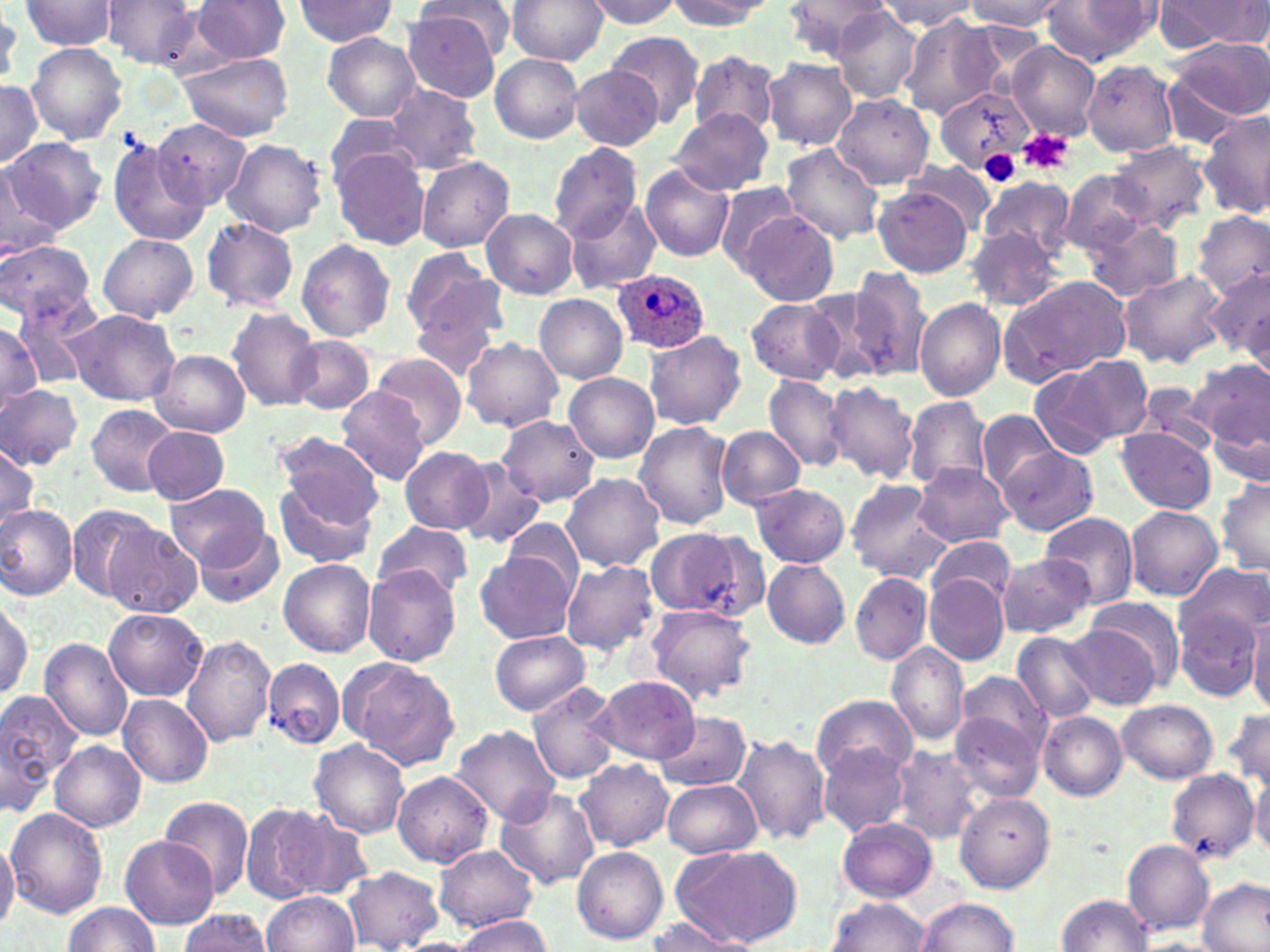

slide_level_diagnosis: Plasmodium ovale
uninfected_red_blood_cell_locations: 'approximate bounding boxes as [x1, y1, x2, y2] in pixels: [19, 0, 120, 53], [102, 0, 199, 67], [192, 0, 289, 62], [294, 0, 396, 45], [418, 0, 519, 52], [506, 0, 608, 64], [583, 0, 679, 27], [663, 0, 769, 31], [782, 0, 891, 59], [881, 0, 976, 30], [963, 0, 1065, 30], [1156, 0, 1268, 51], [1039, 1, 1157, 66], [834, 7, 920, 102], [403, 13, 504, 102], [899, 15, 1004, 118], [323, 31, 422, 122], [607, 32, 703, 126], [1168, 37, 1270, 125], [1005, 41, 1102, 139], [26, 43, 128, 145], [690, 50, 778, 139], [177, 52, 294, 140], [490, 54, 583, 143], [764, 58, 857, 150], [1083, 61, 1179, 157], [568, 65, 663, 151], [0, 80, 45, 171], [387, 84, 481, 174], [937, 87, 1035, 171], [833, 94, 934, 188], [670, 109, 773, 195], [1200, 111, 1270, 221], [324, 115, 414, 190], [152, 119, 252, 211], [106, 133, 208, 251], [3, 136, 103, 234], [223, 139, 326, 237], [548, 143, 644, 239], [778, 143, 885, 246], [1107, 143, 1208, 232], [331, 148, 431, 248], [416, 156, 515, 253], [902, 160, 1000, 233], [640, 165, 735, 261], [0, 168, 61, 258], [1058, 170, 1148, 255], [978, 175, 1073, 258], [712, 183, 804, 270], [873, 186, 973, 278], [564, 195, 661, 295], [481, 209, 578, 299], [1194, 209, 1270, 302], [742, 211, 839, 305], [202, 218, 300, 312], [1081, 220, 1184, 301], [965, 227, 1064, 310], [98, 233, 199, 322], [295, 239, 395, 342], [1, 240, 95, 322], [403, 247, 503, 341], [848, 266, 931, 379], [1206, 267, 1268, 363], [1118, 268, 1228, 369], [1000, 277, 1132, 385], [798, 287, 897, 384], [11, 290, 100, 386], [536, 294, 627, 385], [746, 299, 843, 384], [915, 299, 1006, 401], [408, 302, 502, 382], [228, 307, 321, 410], [64, 309, 180, 406], [0, 320, 41, 417], [645, 331, 746, 430], [287, 335, 375, 414], [461, 338, 564, 433], [153, 350, 250, 436], [373, 353, 467, 450], [1065, 354, 1154, 442], [1191, 359, 1270, 452], [1030, 365, 1123, 460], [566, 374, 659, 463], [763, 375, 852, 472], [821, 382, 918, 483], [0, 383, 83, 469], [1133, 383, 1219, 454], [336, 387, 429, 484], [904, 396, 991, 492], [86, 404, 182, 495], [1207, 406, 1269, 488], [978, 409, 1064, 492], [498, 415, 600, 506], [634, 421, 733, 530], [718, 425, 804, 509], [144, 426, 229, 505], [1116, 429, 1215, 513], [273, 431, 386, 525], [0, 445, 40, 538], [400, 446, 493, 534], [998, 447, 1098, 535], [455, 461, 547, 550], [913, 464, 1012, 547], [562, 472, 663, 571], [274, 479, 378, 568], [844, 479, 951, 583], [1215, 479, 1270, 578], [751, 483, 849, 568], [168, 484, 270, 569], [0, 501, 77, 601], [67, 504, 164, 603], [1125, 505, 1223, 600], [1041, 512, 1138, 610], [501, 519, 586, 596], [372, 520, 473, 601], [104, 522, 202, 617], [196, 526, 284, 607], [645, 529, 745, 615], [688, 532, 772, 621], [928, 535, 1015, 608], [475, 551, 576, 644], [997, 554, 1093, 638], [278, 559, 375, 657], [561, 559, 660, 658], [762, 559, 850, 649], [1176, 561, 1268, 655], [363, 566, 461, 666], [850, 573, 932, 664], [924, 575, 1008, 666], [0, 593, 37, 703], [1087, 594, 1185, 688], [644, 604, 756, 702], [1175, 606, 1261, 702], [105, 608, 208, 700], [1247, 616, 1270, 711], [1068, 622, 1163, 708], [488, 629, 588, 715], [1012, 630, 1101, 724], [183, 635, 277, 747], [41, 639, 133, 740], [887, 642, 969, 746], [264, 658, 345, 749], [345, 659, 459, 772], [954, 671, 1051, 760], [593, 675, 699, 763], [527, 680, 620, 784], [0, 692, 84, 791], [119, 694, 213, 786], [812, 694, 918, 782], [1118, 700, 1218, 782], [1223, 704, 1270, 793], [950, 708, 1044, 800], [654, 711, 751, 791], [1038, 712, 1128, 799], [1, 723, 51, 817], [451, 724, 561, 826], [734, 734, 831, 847], [309, 740, 410, 839], [51, 741, 145, 832], [408, 744, 546, 856], [889, 745, 986, 845], [818, 746, 909, 837], [576, 758, 673, 851], [1168, 770, 1259, 881], [390, 771, 493, 867], [1249, 773, 1270, 859], [660, 778, 761, 860], [495, 786, 601, 890], [955, 793, 1055, 892], [158, 795, 253, 900], [241, 802, 331, 903], [8, 809, 107, 918], [282, 810, 377, 900], [837, 817, 938, 901], [0, 833, 18, 932], [120, 835, 218, 929], [1123, 840, 1213, 935], [671, 842, 801, 949], [432, 844, 539, 932], [572, 845, 668, 944], [344, 866, 441, 950], [1198, 879, 1270, 951], [263, 891, 359, 951], [1056, 895, 1153, 952], [826, 897, 931, 951], [916, 898, 1019, 951], [60, 902, 160, 952], [175, 909, 274, 952], [451, 916, 552, 951], [640, 918, 746, 950]'
magnification: 1000x
platelet_locations: 'approximate bounding boxes as [x1, y1, x2, y2] in pixels: [1016, 128, 1073, 176], [981, 151, 1020, 185]'
field_of_view: single
plasmodium_ovale_infected_red_blood_cell_locations: 'approximate bounding boxes as [x1, y1, x2, y2] in pixels: [614, 268, 709, 353]'
stain: May-Grünwald-Giemsa
image_size: 1270×952 pixels
preparation: thin blood smear
modality: light microscopy